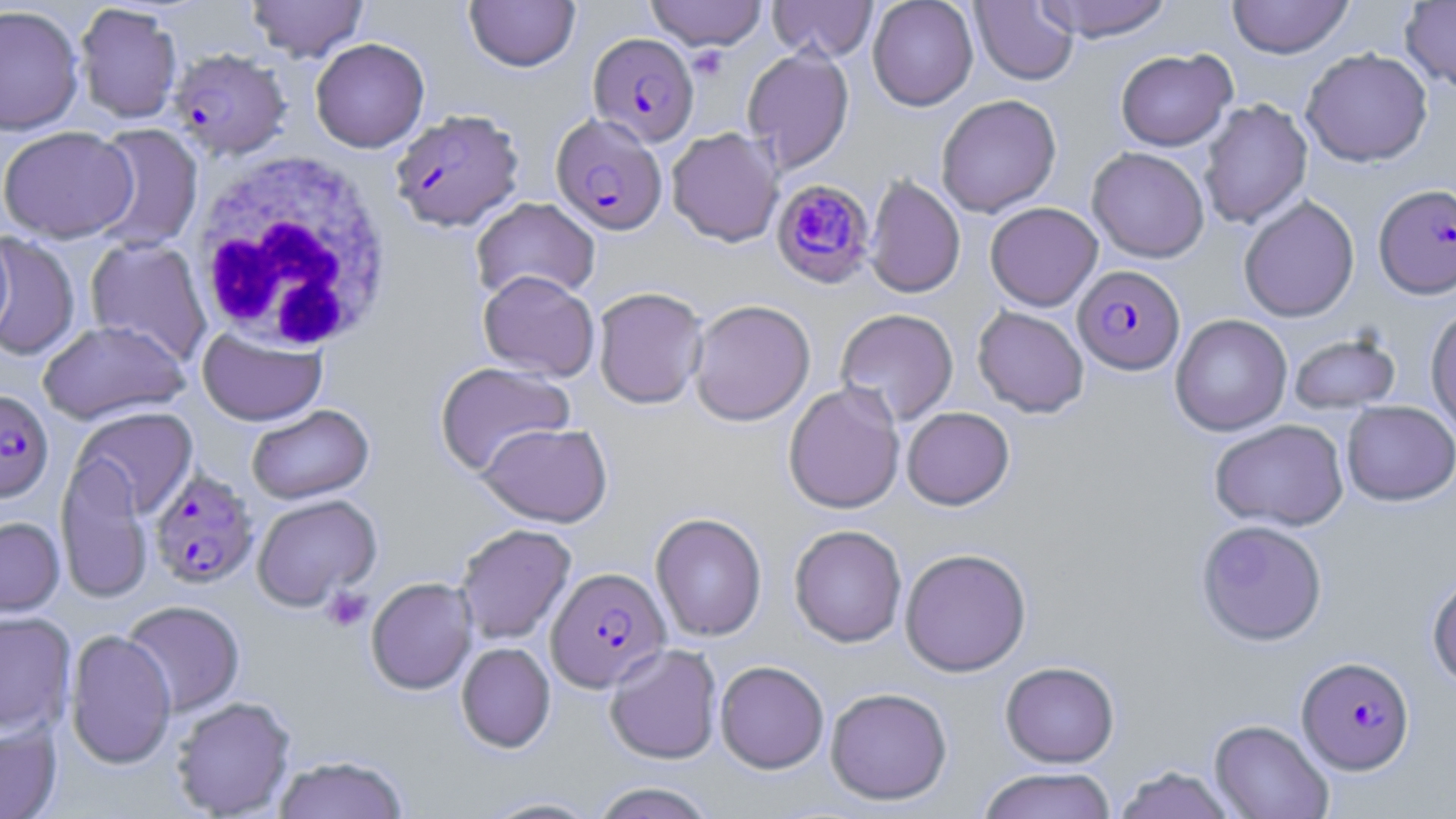
Summary:
  - Coordinate format: approximate bounding boxes as (x1, y1, x2, y2) in pixels
  - Plasmodium falciparum-infected red blood cell locations: (588, 32, 699, 146), (168, 49, 292, 161), (389, 109, 525, 233), (551, 113, 668, 235), (770, 179, 875, 288), (1374, 183, 1456, 299), (1073, 265, 1185, 374), (0, 389, 53, 503), (148, 468, 258, 590), (546, 566, 670, 692), (1297, 656, 1415, 775)
  - Uninfected red blood cell locations: (245, 0, 369, 63), (464, 0, 580, 73), (645, 0, 767, 50), (766, 0, 878, 62), (867, 0, 979, 111), (1034, 0, 1176, 42), (1226, 0, 1354, 59), (1400, 0, 1456, 94), (970, 1, 1079, 85), (74, 4, 182, 126), (0, 6, 85, 138), (310, 38, 430, 153), (742, 46, 855, 173), (1301, 47, 1433, 167), (1115, 49, 1236, 151), (936, 94, 1062, 218), (1198, 99, 1313, 229), (89, 124, 204, 253), (666, 127, 784, 247), (0, 129, 139, 244), (1087, 146, 1210, 263), (864, 175, 966, 298), (1238, 195, 1360, 322), (471, 196, 601, 303), (985, 202, 1103, 311), (0, 232, 15, 344), (0, 233, 81, 362), (84, 237, 212, 366), (478, 270, 600, 382), (593, 286, 708, 409), (689, 299, 816, 426), (972, 306, 1089, 417), (1425, 306, 1456, 438), (835, 308, 959, 426), (1170, 314, 1292, 436), (37, 319, 190, 426), (197, 326, 328, 427), (1288, 331, 1402, 415), (435, 362, 575, 476), (783, 381, 906, 514), (1341, 401, 1456, 506), (247, 405, 373, 505), (72, 407, 198, 519), (901, 407, 1015, 510), (1209, 419, 1349, 531), (477, 422, 612, 527), (55, 453, 155, 605), (252, 494, 382, 611), (650, 512, 767, 642), (0, 516, 65, 620), (1195, 519, 1328, 645), (455, 524, 576, 645), (789, 524, 907, 647), (788, 534, 1030, 653), (899, 548, 1031, 676), (1426, 572, 1456, 689), (366, 577, 478, 695), (121, 600, 245, 717), (0, 611, 77, 735), (64, 629, 177, 770), (456, 642, 556, 753), (604, 643, 722, 764), (715, 660, 829, 773), (1000, 661, 1119, 767), (824, 687, 953, 805), (170, 696, 297, 818), (1209, 719, 1334, 819), (0, 721, 62, 819), (273, 755, 411, 819), (1112, 765, 1237, 819), (976, 768, 1118, 819), (588, 782, 720, 819), (475, 794, 606, 817)
  - Platelet locations: (687, 46, 732, 80), (321, 587, 373, 632)
  - White blood cell locations: (190, 152, 395, 354)
  - Slide-level diagnosis: Plasmodium falciparum
  - Modality: light microscopy
  - Preparation: thin blood film
  - Magnification: 1000x
  - Stain: May-Grünwald-Giemsa
  - Field of view: single
  - Image size: 1456×819 pixels